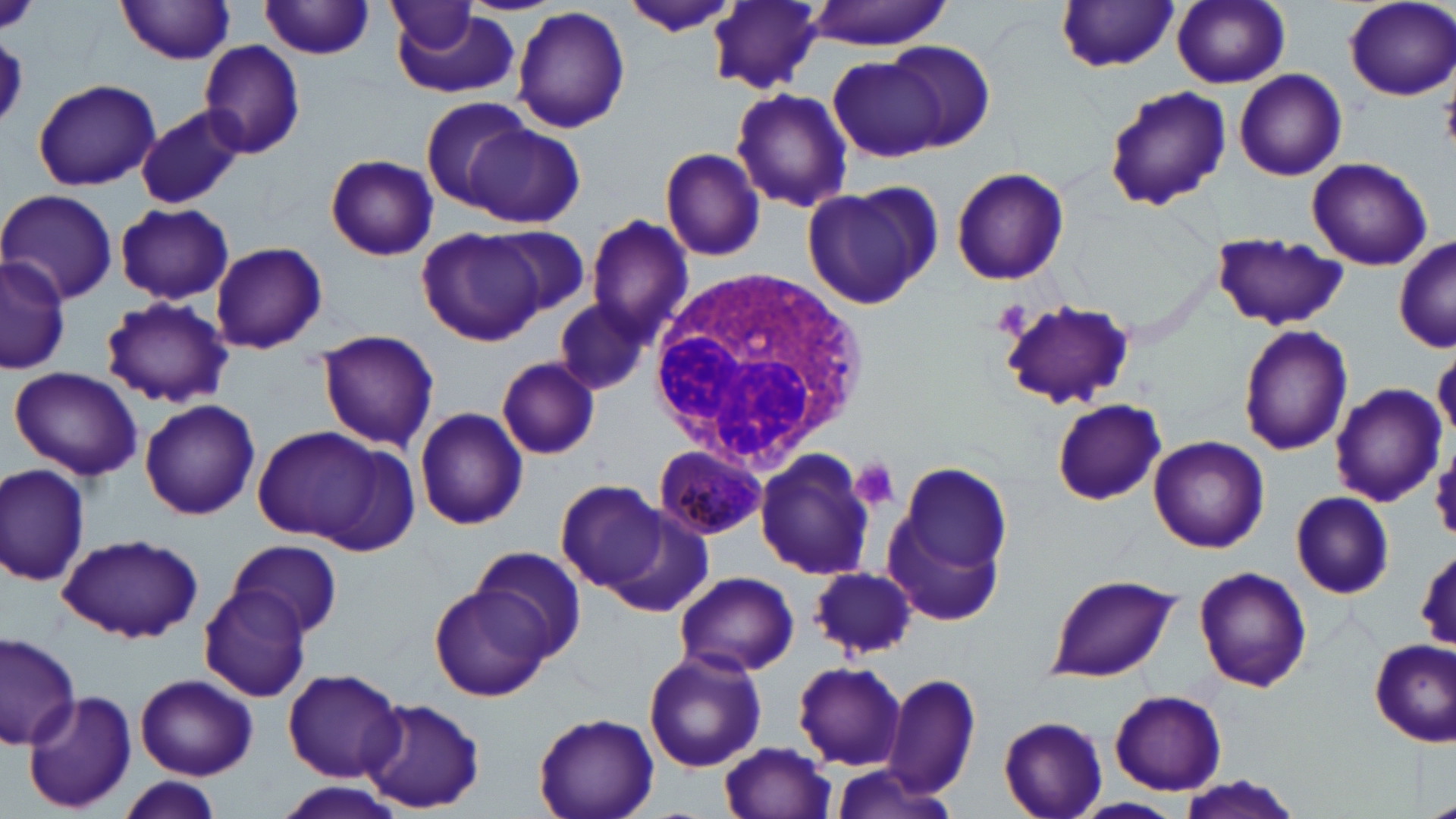
Approximate bounding boxes as (x1, y1, x2, y2) in pixels. White blood cell locations: (650, 268, 874, 478). Plasmodium malariae-infected red blood cell locations: (652, 442, 771, 542). Uninfected red blood cell locations: (116, 0, 237, 64), (705, 0, 827, 93), (1171, 0, 1291, 88), (1342, 0, 1455, 100), (260, 1, 375, 59), (802, 1, 959, 50), (1057, 1, 1178, 72), (620, 2, 742, 38), (388, 3, 476, 51), (511, 5, 632, 136), (389, 8, 519, 99), (197, 40, 306, 159), (885, 40, 996, 151), (830, 57, 949, 161), (1232, 69, 1347, 180), (32, 77, 160, 192), (730, 87, 853, 213), (1104, 87, 1233, 213), (421, 97, 533, 210), (135, 104, 245, 210), (465, 123, 585, 228), (659, 146, 768, 263), (325, 153, 439, 261), (1307, 157, 1433, 271), (950, 167, 1070, 287), (800, 182, 942, 311), (1, 188, 118, 304), (114, 202, 235, 304), (586, 216, 693, 339), (486, 226, 591, 320), (418, 227, 548, 346), (1209, 233, 1349, 332), (1395, 237, 1456, 352), (210, 242, 328, 353), (0, 253, 70, 376), (101, 297, 234, 409), (996, 297, 1136, 411), (554, 299, 655, 396), (1239, 323, 1353, 456), (315, 329, 440, 452), (496, 357, 601, 460), (8, 366, 145, 482), (1330, 382, 1447, 507), (139, 397, 261, 521), (1050, 399, 1165, 505), (414, 406, 529, 530), (248, 425, 404, 548), (1147, 435, 1270, 553), (754, 448, 879, 580), (887, 459, 1015, 616), (1, 464, 90, 587), (556, 478, 668, 593), (1291, 491, 1395, 599), (601, 506, 714, 616), (58, 534, 204, 643), (228, 539, 344, 636), (469, 545, 587, 661), (1415, 549, 1456, 651), (811, 566, 918, 657), (1195, 567, 1312, 692), (675, 570, 799, 678), (1044, 575, 1181, 684), (198, 584, 313, 702), (428, 585, 551, 702), (0, 629, 82, 752), (1369, 640, 1455, 746), (642, 649, 766, 772), (793, 661, 907, 769), (283, 667, 404, 782), (883, 672, 981, 799), (136, 674, 257, 780), (23, 688, 137, 813), (1108, 689, 1229, 795), (361, 698, 484, 814), (532, 710, 660, 819), (998, 716, 1109, 819), (719, 743, 837, 819), (828, 764, 965, 819), (1173, 776, 1307, 818), (118, 777, 223, 819), (275, 782, 404, 819), (1077, 798, 1184, 818). Platelet locations: (992, 299, 1032, 339), (851, 458, 901, 512). Slide-level diagnosis: Plasmodium malariae. May-Grünwald-Giemsa-stained preparation. One field of a larger specimen. Image is 1456×819 pixels. Optical microscopy. 1000x magnification. Thin blood smear.